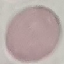

result = no malaria parasites detected
stain = Giemsa
capture = smartphone through the microscope eyepiece
image type = automatically extracted cell patch, resized to 64 × 64 pixels
preparation = thin blood smear